Outline each Plasmodium vivax-infected red blood cell.
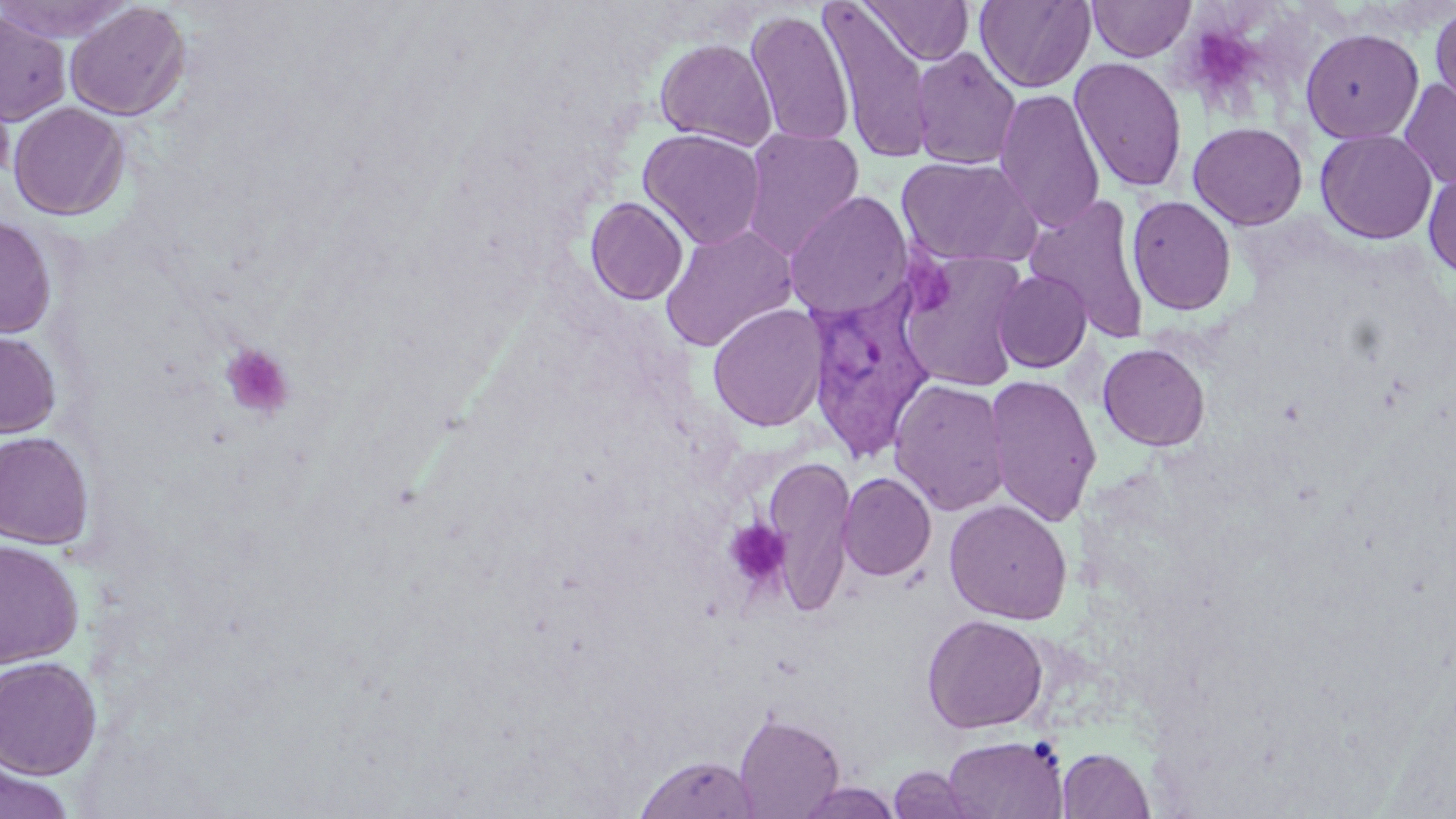

Approximate bounding boxes as [x1, y1, x2, y2] in pixels.
Plasmodium vivax-infected red blood cells: [804, 281, 939, 463].

Platelet locations: [1200, 30, 1256, 94], [901, 254, 955, 313], [220, 343, 295, 420], [723, 519, 792, 590]. Uninfected red blood cell locations: [0, 0, 137, 44], [860, 0, 974, 65], [975, 0, 1096, 93], [1087, 0, 1196, 61], [65, 1, 191, 121], [820, 3, 934, 163], [1429, 4, 1456, 116], [0, 9, 71, 125], [745, 9, 855, 148], [1300, 27, 1424, 144], [654, 38, 777, 150], [910, 47, 1021, 170], [1070, 56, 1188, 194], [0, 75, 16, 184], [1398, 78, 1456, 190], [994, 88, 1106, 232], [8, 101, 130, 220], [1188, 121, 1308, 230], [638, 128, 767, 250], [740, 128, 865, 259], [1315, 129, 1437, 244], [896, 155, 1041, 268], [1423, 167, 1456, 280], [783, 191, 913, 321], [1026, 195, 1152, 342], [1127, 195, 1237, 315], [585, 197, 688, 305], [0, 215, 57, 339], [659, 224, 798, 352], [895, 250, 1032, 392], [991, 269, 1092, 373], [707, 303, 829, 432], [0, 329, 62, 438], [1097, 343, 1210, 451], [983, 374, 1102, 526], [888, 378, 1011, 516], [0, 431, 95, 549], [762, 454, 856, 616], [837, 472, 936, 582], [944, 499, 1073, 624], [0, 539, 83, 667], [921, 613, 1049, 734], [0, 655, 103, 778], [733, 711, 845, 818], [941, 734, 1068, 818], [1057, 747, 1155, 818], [634, 754, 760, 819], [0, 757, 75, 819], [887, 765, 988, 819], [794, 781, 904, 819]. Slide-level diagnosis: Plasmodium vivax. Captured at 1000x magnification. Optical microscopy. Single field of view. May-Grünwald-Giemsa stain. Thin blood smear. Image is 1456×819 pixels.